Report the malaria status of this cell.
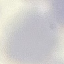
It is uninfected.

stain = Giemsa
preparation = thin smear
capture = smartphone camera at the microscope eyepiece
image type = cell patch, automatically extracted from a larger field of view and resized to 64 × 64 pixels